Locate every Plasmodium parasite and every leukocyte.
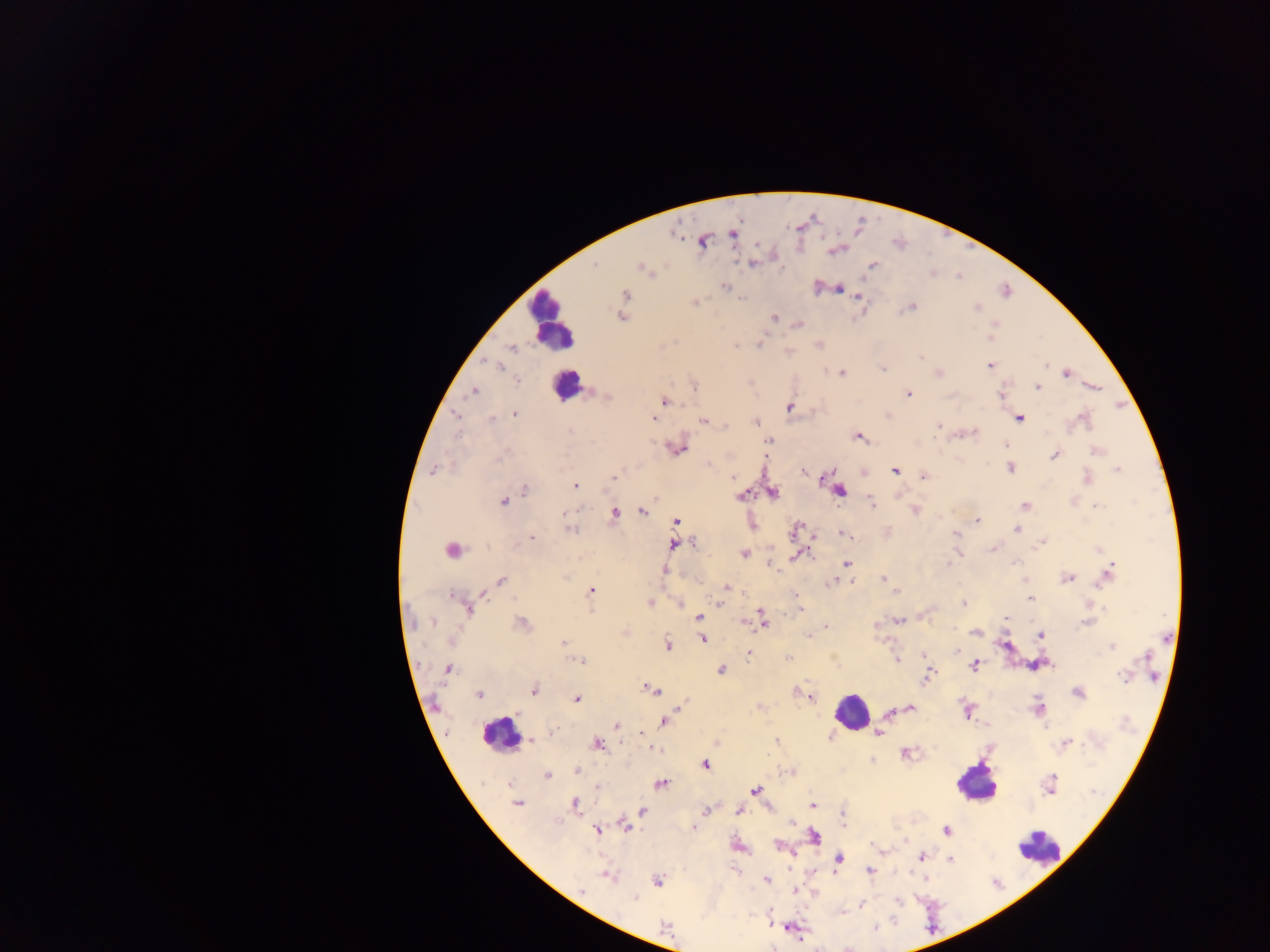

Approximate centers as {x, y} in pixels.
Plasmodium parasites: {734, 236}, {703, 242}, {834, 251}, {595, 264}, {872, 265}, {643, 269}, {725, 286}, {840, 289}, {624, 294}, {857, 297}, {694, 302}, {912, 307}, {976, 308}, {621, 317}, {774, 318}, {779, 320}, {799, 324}, {994, 325}, {990, 338}, {759, 343}, {736, 346}, {512, 348}, {920, 357}, {989, 365}, {1045, 365}, {501, 366}, {883, 369}, {842, 372}, {939, 373}, {1066, 373}, {518, 381}, {695, 386}, {1038, 387}, {473, 391}, {908, 394}, {1002, 396}, {607, 397}, {663, 401}, {789, 407}, {514, 414}, {456, 415}, {888, 415}, {496, 418}, {653, 419}, {1020, 419}, {1084, 419}, {491, 420}, {704, 421}, {756, 422}, {724, 425}, {939, 426}, {570, 429}, {973, 433}, {858, 436}, {769, 441}, {1006, 444}, {678, 449}, {1098, 450}, {1054, 455}, {1011, 468}, {435, 469}, {1117, 469}, {894, 471}, {803, 472}, {613, 477}, {732, 477}, {923, 477}, {1086, 478}, {575, 486}, {525, 489}, {840, 491}, {774, 492}, {741, 496}, {655, 498}, {503, 501}, {871, 503}, {1025, 506}, {1096, 506}, {916, 511}, {642, 512}, {564, 513}, {615, 513}, {977, 521}, {676, 522}, {797, 527}, {570, 530}, {1016, 530}, {843, 534}, {955, 534}, {531, 538}, {1041, 542}, {695, 544}, {672, 545}, {993, 549}, {451, 550}, {1099, 550}, {800, 553}, {744, 554}, {949, 562}, {1017, 562}, {846, 563}, {772, 566}, {1111, 568}, {663, 571}, {1107, 574}, {565, 577}, {1067, 578}, {883, 579}, {501, 581}, {834, 582}, {851, 582}, {726, 587}, {591, 591}, {452, 595}, {796, 596}, {1030, 599}, {650, 603}, {719, 603}, {963, 603}, {681, 604}, {799, 608}, {468, 609}, {591, 612}, {699, 616}, {1007, 618}, {898, 620}, {1087, 621}, {432, 622}, {763, 622}, {522, 623}, {876, 626}, {826, 627}, {624, 633}, {976, 633}, {808, 636}, {1041, 636}, {702, 639}, {564, 642}, {668, 644}, {1112, 647}, {958, 650}, {748, 653}, {925, 654}, {1146, 657}, {788, 658}, {897, 659}, {580, 661}, {974, 666}, {1038, 666}, {447, 669}, {721, 670}, {928, 676}, {1123, 677}, {533, 689}, {651, 690}, {1078, 692}, {479, 695}, {809, 696}, {577, 699}, {685, 702}, {682, 706}, {1038, 707}, {911, 708}, {967, 711}, {663, 721}, {616, 726}, {1045, 726}, {553, 732}, {641, 732}, {878, 733}, {531, 740}, {776, 740}, {1068, 743}, {598, 744}, {655, 750}, {906, 754}, {705, 765}, {577, 771}, {791, 773}, {547, 776}, {661, 784}, {510, 785}, {1050, 785}, {597, 787}, {755, 791}, {517, 803}, {575, 803}, {812, 805}, {705, 811}, {739, 811}, {643, 812}, {843, 824}, {624, 825}, {694, 828}, {597, 830}, {947, 830}, {814, 836}, {780, 846}, {921, 856}, {839, 859}, {950, 860}, {870, 870}, {607, 875}, {657, 880}, {767, 880}, {582, 890}, {797, 891}, {636, 898}, {898, 902}, {861, 904}, {666, 927}.
Leukocytes: {551, 323}, {567, 386}, {851, 711}, {500, 732}, {977, 785}, {1040, 850}.

{
  "preparation": "thick blood film",
  "country": "Ghana",
  "capture": "mobile-phone photograph through a microscope",
  "image_size": "1270×952 pixels",
  "field_of_view": "single"
}